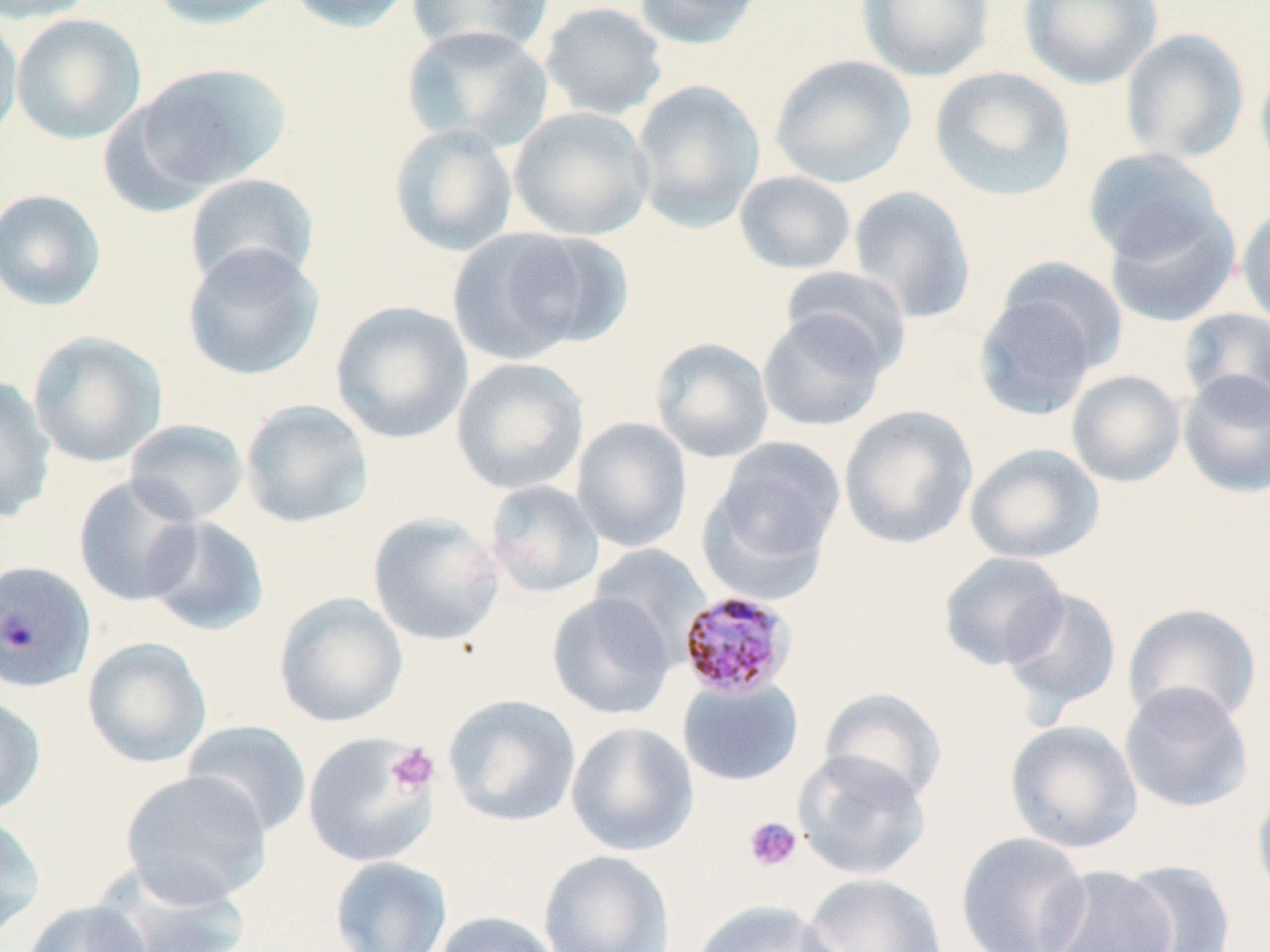
Approximate bounding boxes as [x1, y1, x2, y2] in pixels. Platelet locations: [386, 743, 439, 795], [743, 816, 803, 872]. Uninfected red blood cell locations: [0, 0, 99, 24], [144, 0, 293, 30], [284, 0, 414, 33], [631, 0, 768, 49], [856, 0, 995, 83], [1019, 0, 1163, 90], [406, 1, 555, 59], [538, 1, 669, 121], [0, 10, 24, 145], [10, 13, 147, 145], [401, 24, 553, 152], [1120, 28, 1250, 165], [769, 53, 917, 189], [1254, 58, 1270, 182], [131, 62, 292, 194], [929, 66, 1078, 203], [629, 80, 767, 231], [508, 106, 656, 241], [388, 124, 519, 257], [1081, 147, 1226, 265], [734, 170, 857, 275], [183, 172, 321, 290], [848, 184, 977, 325], [0, 188, 107, 312], [1103, 200, 1241, 328], [1236, 201, 1270, 331], [445, 226, 615, 364], [181, 243, 324, 381], [994, 256, 1130, 379], [780, 266, 911, 376], [974, 283, 1106, 419], [330, 301, 474, 444], [1178, 307, 1270, 417], [757, 310, 891, 433], [27, 330, 168, 468], [650, 337, 775, 464], [451, 357, 589, 495], [1066, 369, 1186, 488], [1177, 370, 1270, 498], [0, 376, 57, 524], [239, 399, 374, 529], [839, 404, 979, 550], [572, 416, 693, 553], [123, 419, 250, 526], [700, 441, 846, 595], [965, 443, 1105, 564], [73, 475, 203, 606], [483, 480, 605, 599], [367, 512, 505, 647], [142, 515, 270, 637], [590, 544, 710, 659], [938, 551, 1070, 671], [1000, 587, 1123, 722], [273, 592, 408, 728], [546, 592, 676, 721], [1122, 602, 1264, 729], [81, 637, 212, 768], [677, 677, 804, 787], [1118, 681, 1254, 815], [819, 687, 947, 806], [442, 693, 581, 827], [0, 695, 46, 817], [1004, 719, 1144, 854], [180, 720, 313, 838], [566, 721, 699, 856], [302, 732, 438, 868], [793, 749, 932, 881], [120, 770, 272, 907], [1251, 780, 1270, 908], [0, 811, 47, 940], [955, 831, 1092, 952], [539, 849, 674, 952], [329, 855, 452, 952], [1116, 859, 1238, 952], [92, 863, 250, 952], [1038, 864, 1177, 952], [801, 872, 950, 952], [689, 899, 841, 952], [21, 900, 154, 952], [432, 910, 563, 952]. Plasmodium malariae-infected red blood cell locations: [0, 561, 97, 694], [684, 593, 803, 703]. Slide-level diagnosis: Plasmodium malariae. Light microscopy. May-Grünwald-Giemsa-stained preparation. Captured at 1000x magnification. One field of a larger specimen. Thin blood film. Image is 1270×952 pixels.